Identify the blood parasite species.
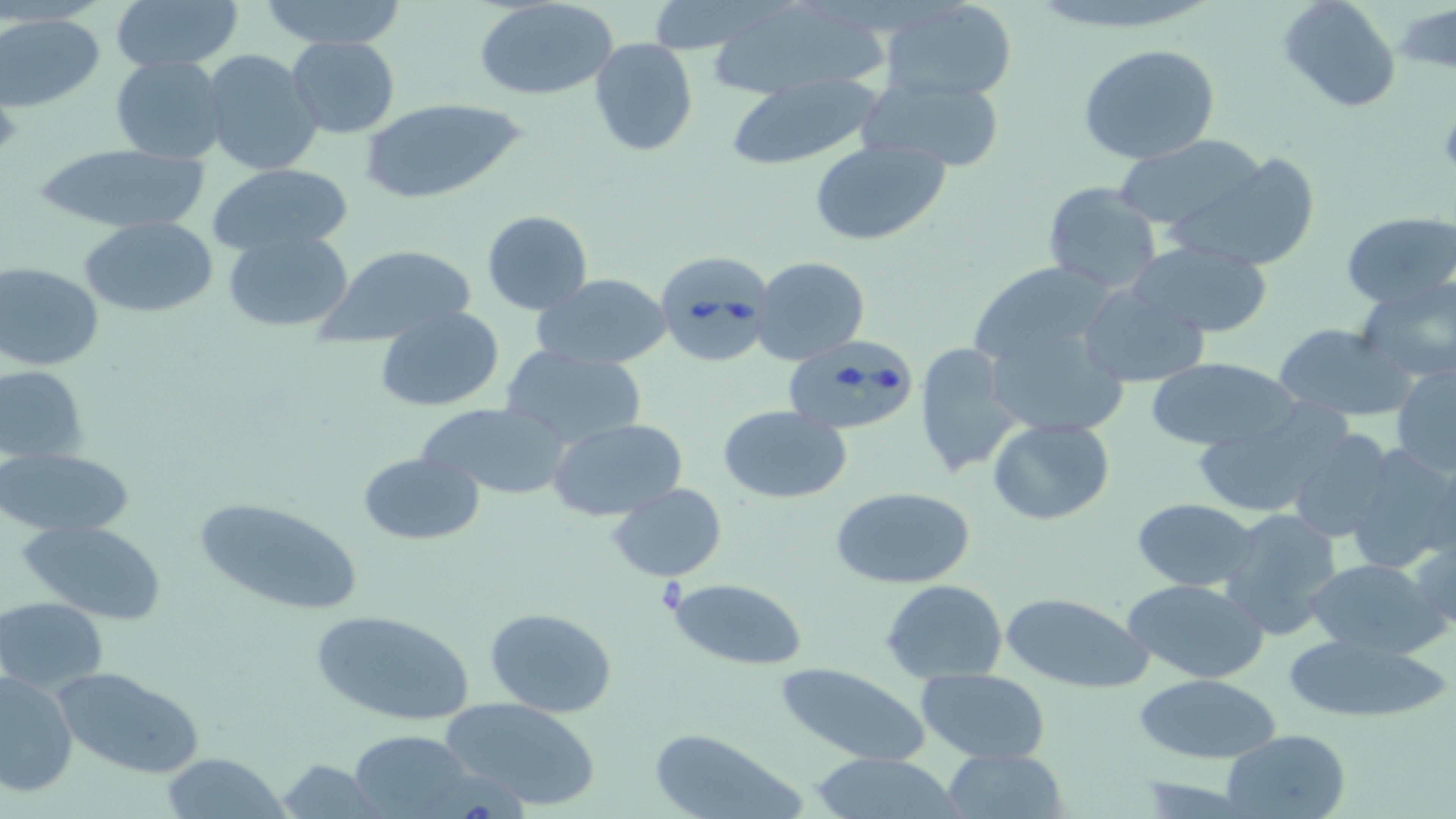

Babesia divergens.

Approximate bounding boxes as [x1, y1, x2, y2] in pixels. Babesia divergens-infected red blood cell locations: [660, 250, 781, 367], [775, 340, 916, 455]. Uninfected red blood cell locations: [111, 0, 241, 73], [262, 0, 408, 51], [474, 0, 622, 101], [1278, 0, 1401, 113], [880, 1, 1019, 102], [708, 2, 886, 101], [1, 14, 104, 112], [286, 35, 400, 138], [589, 38, 698, 156], [1078, 44, 1220, 164], [202, 49, 323, 176], [111, 54, 227, 164], [726, 74, 884, 168], [859, 76, 1005, 169], [358, 98, 526, 204], [1113, 135, 1265, 231], [809, 139, 951, 247], [34, 144, 210, 234], [1169, 148, 1321, 271], [207, 163, 353, 256], [1042, 181, 1161, 294], [481, 212, 593, 314], [1342, 212, 1456, 310], [81, 215, 219, 319], [221, 229, 354, 335], [1128, 241, 1274, 338], [316, 245, 475, 348], [752, 256, 871, 365], [965, 260, 1122, 371], [1, 263, 104, 372], [534, 274, 673, 370], [1358, 280, 1456, 383], [1078, 285, 1209, 387], [375, 306, 505, 412], [981, 322, 1132, 439], [1273, 323, 1412, 421], [914, 342, 1022, 479], [502, 347, 646, 449], [1146, 358, 1303, 452], [1392, 360, 1456, 477], [1, 364, 89, 464], [419, 403, 572, 500], [720, 404, 851, 504], [1185, 410, 1347, 519], [986, 417, 1114, 526], [547, 419, 688, 522], [1286, 431, 1397, 543], [1344, 442, 1456, 575], [0, 447, 134, 537], [359, 451, 484, 547], [608, 485, 729, 580], [829, 485, 978, 589], [191, 495, 366, 615], [1132, 498, 1260, 592], [1221, 509, 1345, 640], [20, 519, 168, 624], [1410, 528, 1455, 636], [1304, 558, 1444, 661], [664, 576, 807, 669], [1121, 578, 1270, 683], [881, 579, 1008, 683], [1000, 592, 1152, 694], [1, 596, 108, 694], [484, 606, 619, 716], [310, 609, 477, 729], [1282, 634, 1453, 725], [775, 662, 932, 767], [53, 665, 201, 778], [916, 667, 1051, 765], [0, 669, 78, 799], [1135, 673, 1286, 762], [439, 696, 601, 811], [348, 729, 474, 816], [648, 729, 798, 818], [1223, 729, 1351, 818], [942, 747, 1068, 818], [159, 754, 293, 818], [808, 754, 965, 818], [278, 760, 381, 817]. May-Grünwald-Giemsa stain. Image is 1456×819 pixels. Optical microscopy. Captured at 1000x magnification. One field of a larger specimen. Thin blood smear.